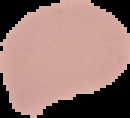

Summary:
  - Image type: cell region segmented out of the field of view; surrounding area masked to black
  - Malaria status: uninfected
  - Image size: 130×118 pixels
  - Preparation: thin blood film